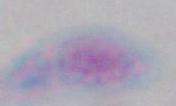
Summary:
  - Modality: micrograph
  - Magnification: 1000x
  - Identification: Toxoplasma gondii